Locate every parasitized RBC.
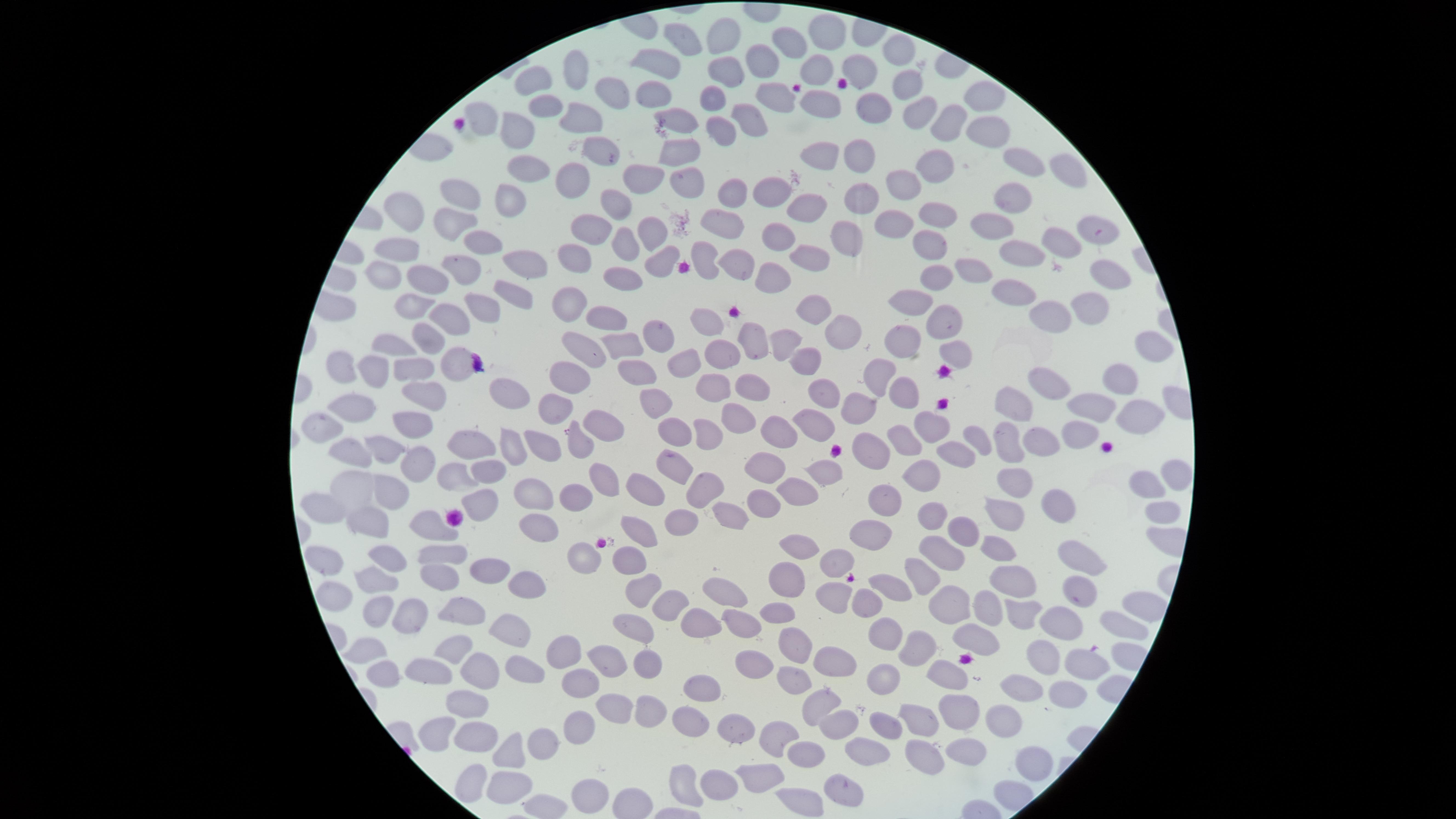
No parasitized RBCs identified.

uninfected_RBCs: 'approximate marker points as (x, y) in pixels: (719, 34), (821, 37), (684, 42), (783, 43), (895, 51), (761, 63), (656, 66), (860, 66), (817, 67), (576, 68), (722, 70), (537, 81), (910, 85), (611, 93), (651, 95), (980, 95), (715, 99), (869, 102), (544, 104), (771, 104), (821, 105), (581, 114), (920, 114), (480, 115), (949, 121), (744, 122), (672, 126), (512, 132), (719, 132), (987, 132), (595, 145), (810, 150), (678, 153), (860, 154), (939, 159), (1024, 162), (526, 163), (1065, 171), (642, 180), (680, 181), (569, 182), (899, 183), (735, 186), (764, 190), (464, 195), (862, 196), (507, 197), (1011, 198), (805, 201), (619, 203), (405, 210), (936, 212), (899, 218), (721, 220), (986, 225), (650, 226), (449, 228), (586, 228), (1093, 229), (775, 234), (846, 234), (1060, 241), (621, 243), (480, 245), (401, 246), (929, 248), (730, 254), (808, 255), (1021, 255), (578, 256), (659, 262), (526, 264), (463, 266), (970, 267), (627, 272), (380, 273), (427, 273), (1108, 275), (770, 278), (929, 280), (1011, 289), (514, 291), (407, 303), (565, 303), (906, 305), (480, 307), (1086, 307), (813, 312), (941, 314), (1049, 314), (448, 315), (610, 319), (708, 320), (843, 328), (651, 333), (787, 333), (754, 336), (427, 339), (614, 341), (901, 342), (394, 344), (1148, 345), (582, 348), (958, 349), (806, 356), (719, 357), (449, 362), (406, 366), (687, 367), (343, 369), (633, 370), (376, 374), (573, 374), (879, 378), (1111, 378), (1052, 383), (743, 384), (716, 390), (424, 391), (505, 391), (821, 392), (895, 392), (650, 400), (861, 403), (1012, 403), (354, 407), (1083, 408), (1132, 411), (548, 415), (737, 417), (405, 420), (595, 421), (927, 422), (326, 423), (812, 425), (771, 429), (706, 430), (675, 434), (1071, 438), (580, 439), (976, 439), (1035, 444), (388, 445), (538, 445), (473, 446), (896, 446), (954, 446), (1004, 446), (507, 448), (871, 452), (348, 454), (671, 459), (407, 461), (818, 467), (759, 470), (487, 472), (449, 474), (920, 474), (1170, 475), (602, 479), (1013, 482), (1149, 482), (354, 490), (387, 490), (700, 491), (797, 491), (651, 494), (577, 495), (538, 497), (878, 502), (1058, 502), (762, 504), (476, 507), (323, 511), (1155, 511), (729, 515), (928, 515), (1003, 515), (681, 522), (368, 524), (537, 526), (645, 529), (962, 532), (431, 533), (866, 535), (995, 540), (802, 544), (941, 550), (442, 552), (381, 555), (580, 557), (839, 558), (1076, 560), (629, 563), (322, 565), (913, 573), (492, 575), (787, 576), (1011, 578), (439, 579), (370, 583), (527, 583), (879, 586), (718, 587), (638, 588), (837, 590), (1071, 591), (331, 599), (863, 601), (663, 607), (950, 607), (980, 607), (403, 613), (1020, 613), (460, 615), (775, 615), (372, 616), (737, 618), (694, 623), (1062, 623), (1115, 623), (505, 627), (630, 628), (879, 631), (974, 640), (795, 643), (364, 644), (457, 646), (925, 649), (559, 651), (835, 658), (605, 660), (1077, 660), (1039, 661), (645, 662), (751, 663), (431, 665), (380, 667), (479, 668), (518, 669), (951, 673), (884, 674), (799, 679), (583, 683), (703, 684), (1019, 691), (1063, 691), (469, 703), (615, 706), (816, 706), (652, 710), (955, 715), (688, 718), (834, 719), (919, 721), (999, 723), (881, 724), (579, 728), (734, 732), (470, 735), (427, 738), (775, 738), (546, 743), (518, 748), (971, 749), (871, 752), (804, 756), (918, 758), (1032, 764), (762, 771), (511, 781), (721, 781), (470, 782), (847, 783), (585, 796), (804, 798)'
image_size: 1456×819 pixels
capture: smartphone photograph through the microscope eyepiece
visible_region: circular
preparation: thin blood smear
stain: Giemsa
field_of_view: single